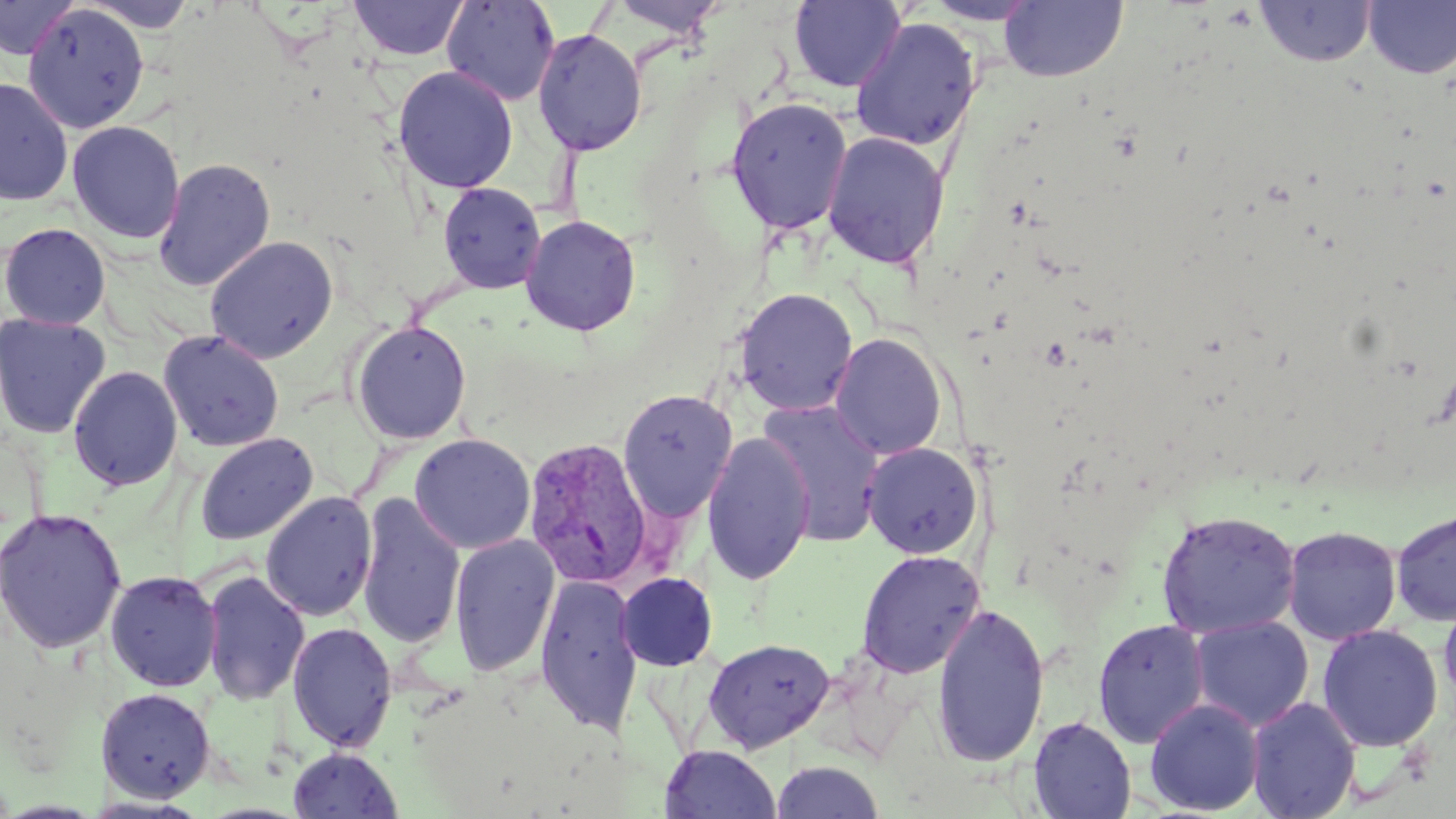
slide-level diagnosis = Plasmodium vivax
image size = 1456×819 pixels
Plasmodium vivax-infected red blood cell locations = approximate bounding boxes as (x1,y1)-(x2,y2) corner pairs in pixels: (523,436)-(655,590)
modality = optical microscopy
magnification = 1000x
uninfected red blood cell locations = approximate bounding boxes as (x1,y1)-(x2,y2) corner pairs in pixels: (0,0)-(79,61), (441,0)-(561,106), (608,0)-(728,37), (923,0)-(1044,25), (349,1)-(469,61), (789,1)-(906,92), (1000,1)-(1128,83), (1255,1)-(1376,67), (1363,1)-(1456,79), (75,2)-(203,33), (21,5)-(150,134), (850,17)-(982,152), (532,29)-(647,156), (393,66)-(518,194), (0,76)-(74,206), (726,97)-(853,236), (67,121)-(185,244), (822,131)-(949,270), (153,158)-(276,291), (438,182)-(546,294), (521,215)-(641,336), (0,222)-(111,330), (204,236)-(339,363), (733,287)-(858,416), (1,312)-(112,438), (350,320)-(472,444), (158,330)-(284,452), (830,332)-(948,461), (68,365)-(183,491), (617,389)-(737,522), (755,399)-(887,546), (195,432)-(318,545), (701,432)-(815,585), (409,433)-(535,554), (861,442)-(983,559), (260,491)-(378,621), (357,492)-(466,649), (0,507)-(127,654), (1390,509)-(1456,626), (1156,510)-(1301,639), (1282,526)-(1402,644), (450,534)-(559,676), (857,550)-(984,678), (105,569)-(222,692), (201,569)-(310,706), (616,572)-(718,671), (535,573)-(643,735), (1439,599)-(1456,709), (931,603)-(1050,769), (1189,616)-(1314,731), (1092,619)-(1210,748), (287,621)-(397,752), (1317,624)-(1443,752), (703,637)-(834,753), (96,686)-(216,803), (1247,697)-(1362,819), (1145,698)-(1264,816), (1028,716)-(1137,818), (660,745)-(781,818), (288,747)-(403,818), (770,760)-(886,818)
field of view = single
stain = May-Grünwald-Giemsa
preparation = thin blood film